Describe the morphology of the red blood cells.
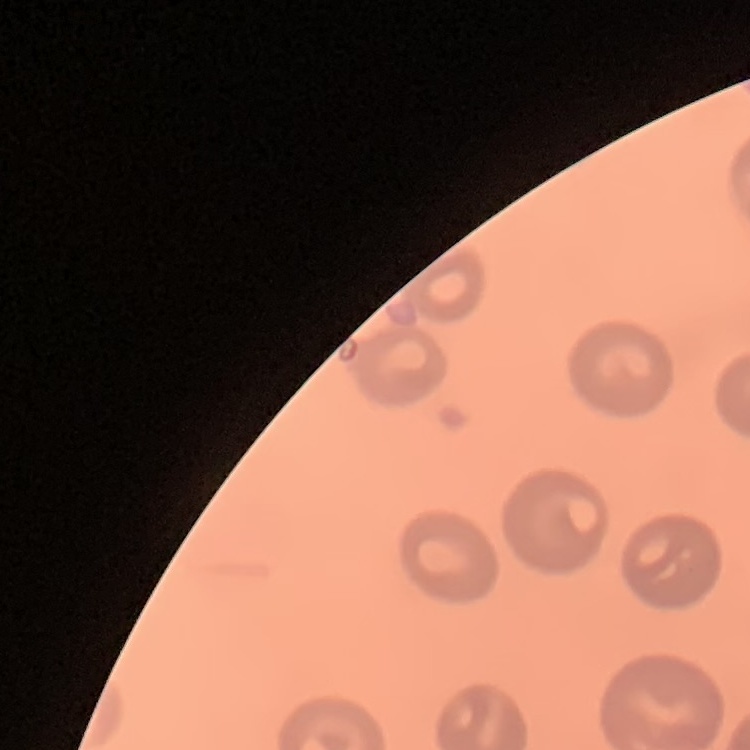

They show no rouleaux formation.

image type = one tile cut from a larger photomicrograph
stain = Field's or Giemsa
preparation = thin blood smear